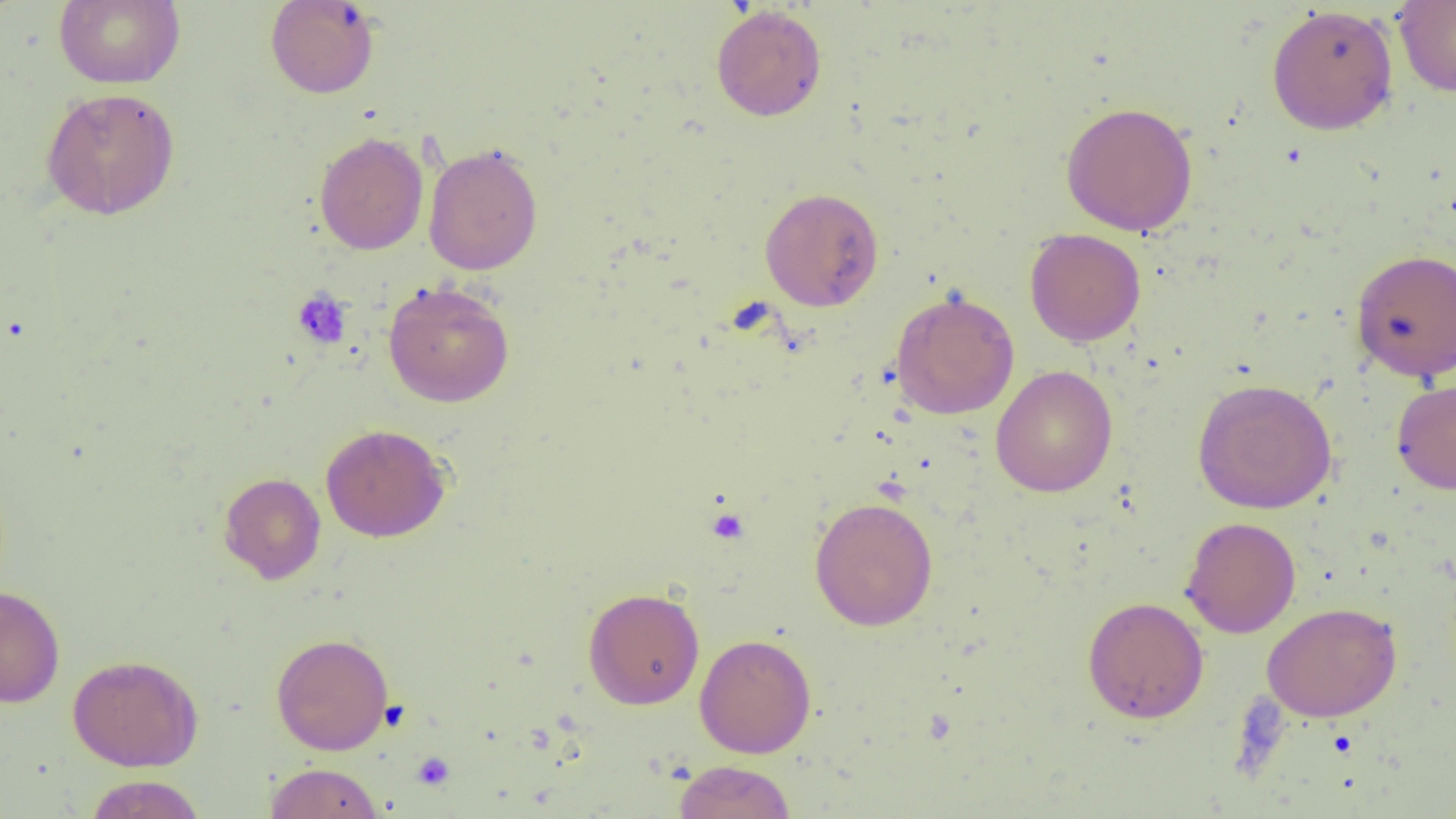
{
  "slide_level_diagnosis": "no evidence of blood parasites",
  "modality": "optical microscopy",
  "preparation": "thin blood smear",
  "platelet_locations": "approximate bounding boxes as (x1,y1)-(x2,y2) corner pairs in pixels: (292,289)-(352,349), (707,507)-(750,544), (1328,730)-(1358,759), (412,752)-(455,790)",
  "magnification": "1000x",
  "uninfected_red_blood_cell_locations": "approximate bounding boxes as (x1,y1)-(x2,y2) corner pairs in pixels: (53,0)-(186,89), (265,1)-(380,99), (1394,1)-(1456,98), (710,4)-(827,121), (1266,4)-(1399,135), (41,87)-(180,220), (1060,101)-(1199,236), (314,131)-(429,255), (423,142)-(543,276), (759,187)-(884,311), (1024,228)-(1146,347), (1350,248)-(1456,382), (383,280)-(515,407), (890,290)-(1020,420), (991,365)-(1118,497), (1192,377)-(1338,514), (1391,379)-(1456,494), (320,423)-(450,543), (219,472)-(326,584), (810,496)-(938,631), (1180,516)-(1301,638), (0,585)-(65,708), (583,587)-(705,709), (1082,596)-(1209,723), (1262,601)-(1402,721), (271,632)-(394,755), (694,633)-(816,758), (67,653)-(203,772), (673,760)-(797,819), (264,762)-(383,819), (84,775)-(206,818)",
  "image_size": "1456×819 pixels",
  "field_of_view": "one of a larger specimen"
}